Assess the morphology of the erythrocytes.
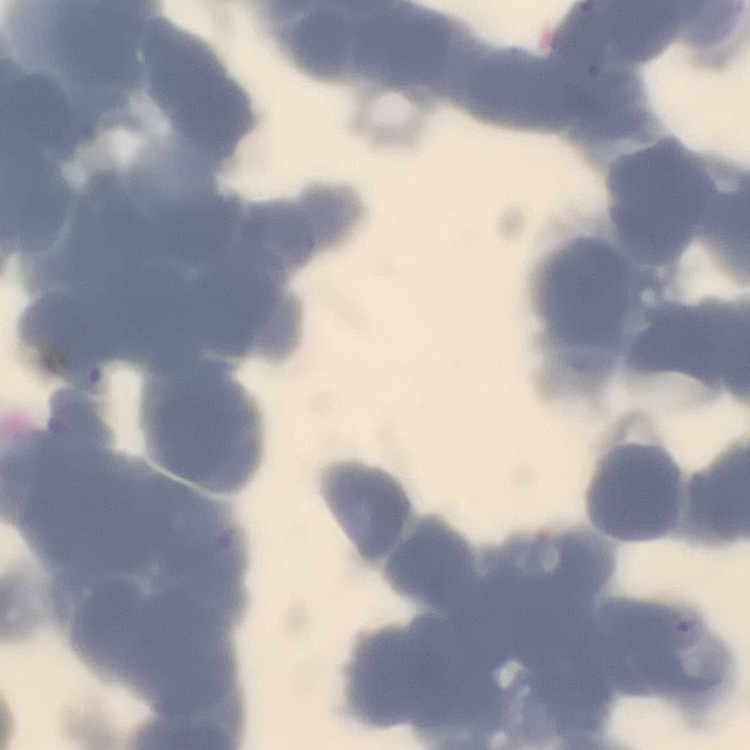
Rouleaux formation.

stain = Field's or Giemsa
image type = square crop of a larger photomicrograph
preparation = thin peripheral smear